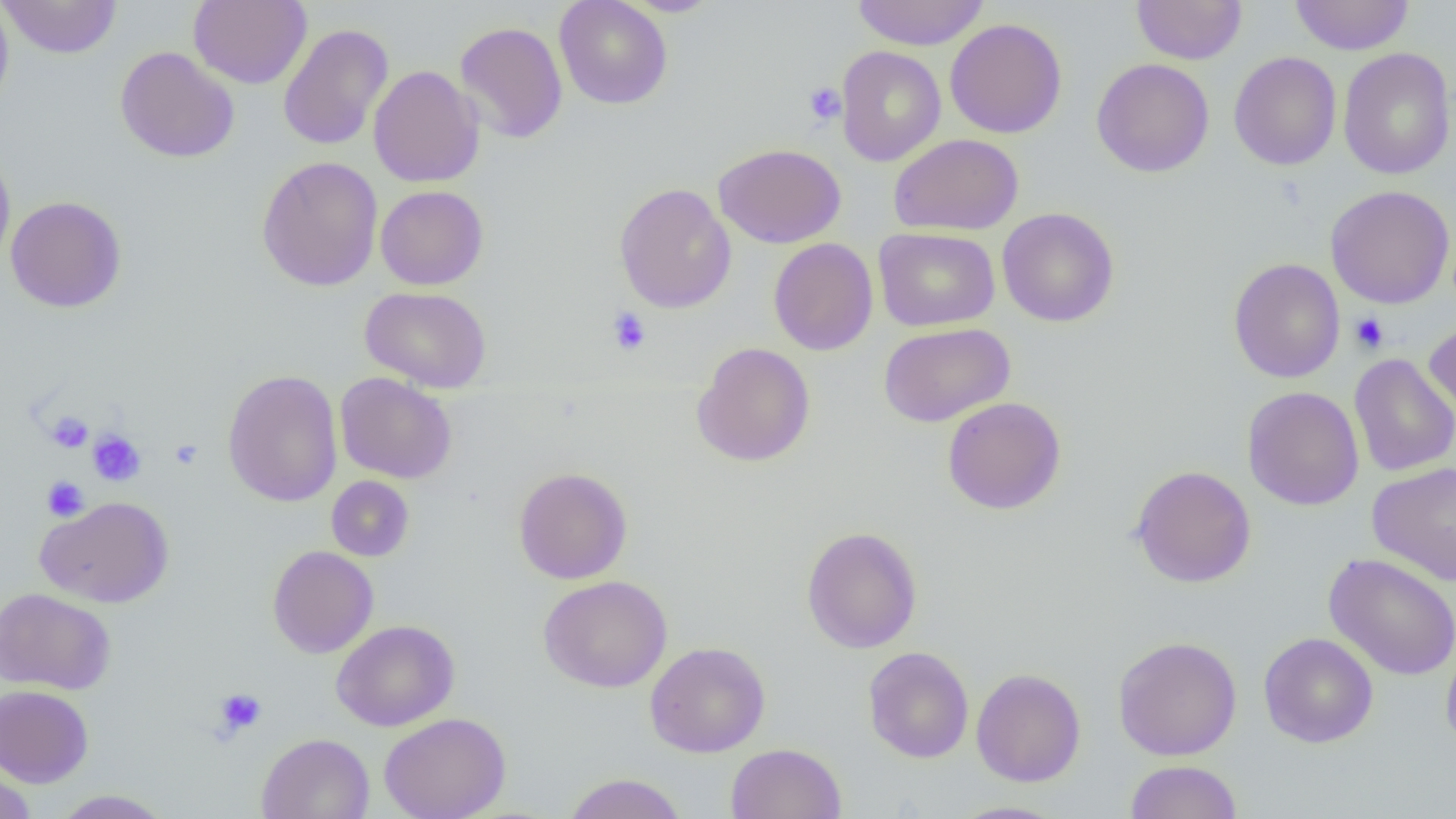

slide-level diagnosis = negative for blood parasites
preparation = thin blood film
platelet locations = approximate bounding boxes as (x1, y1, x2, y2) in pixels: (803, 82, 846, 126), (607, 307, 652, 355), (1350, 313, 1389, 353), (46, 411, 93, 453), (87, 430, 147, 487), (170, 439, 203, 469), (42, 476, 89, 521), (212, 687, 267, 737)
magnification = 1000x
uninfected red blood cell locations = approximate bounding boxes as (x1, y1, x2, y2) in pixels: (0, 0, 14, 114), (1, 0, 122, 59), (189, 0, 312, 89), (554, 0, 673, 109), (620, 0, 723, 16), (851, 0, 989, 50), (1131, 0, 1247, 65), (1289, 0, 1415, 55), (945, 18, 1067, 139), (454, 21, 568, 144), (278, 23, 393, 151), (836, 45, 945, 167), (115, 46, 240, 163), (1338, 47, 1456, 180), (1229, 51, 1341, 170), (1091, 58, 1215, 177), (368, 65, 484, 188), (889, 133, 1024, 235), (714, 143, 845, 248), (0, 147, 16, 272), (257, 155, 383, 291), (614, 183, 737, 313), (375, 185, 489, 290), (1325, 185, 1455, 309), (5, 195, 127, 313), (997, 208, 1120, 327), (874, 227, 999, 331), (768, 238, 878, 356), (1228, 257, 1345, 383), (360, 286, 492, 393), (1424, 317, 1456, 422), (878, 322, 1015, 427), (692, 342, 816, 467), (1349, 353, 1456, 477), (222, 369, 343, 507), (335, 372, 457, 484), (1242, 386, 1364, 510), (942, 396, 1066, 515), (1367, 460, 1456, 585), (1130, 465, 1256, 588), (513, 466, 633, 584), (326, 476, 414, 561), (35, 495, 174, 608), (802, 526, 923, 654), (267, 545, 379, 658), (1323, 553, 1456, 680), (538, 575, 673, 693), (0, 587, 115, 694), (331, 620, 460, 731), (1259, 632, 1378, 748), (1113, 636, 1242, 760), (645, 641, 770, 757), (1441, 642, 1456, 752), (862, 646, 975, 763), (863, 659, 1084, 771), (971, 668, 1086, 787), (0, 684, 94, 787), (379, 712, 511, 819), (257, 732, 375, 819), (725, 742, 847, 819), (1125, 760, 1243, 819), (0, 766, 37, 819), (562, 772, 687, 819), (51, 790, 173, 818), (947, 800, 1068, 819)
field of view = one of a larger specimen
modality = light microscopy
image size = 1456×819 pixels